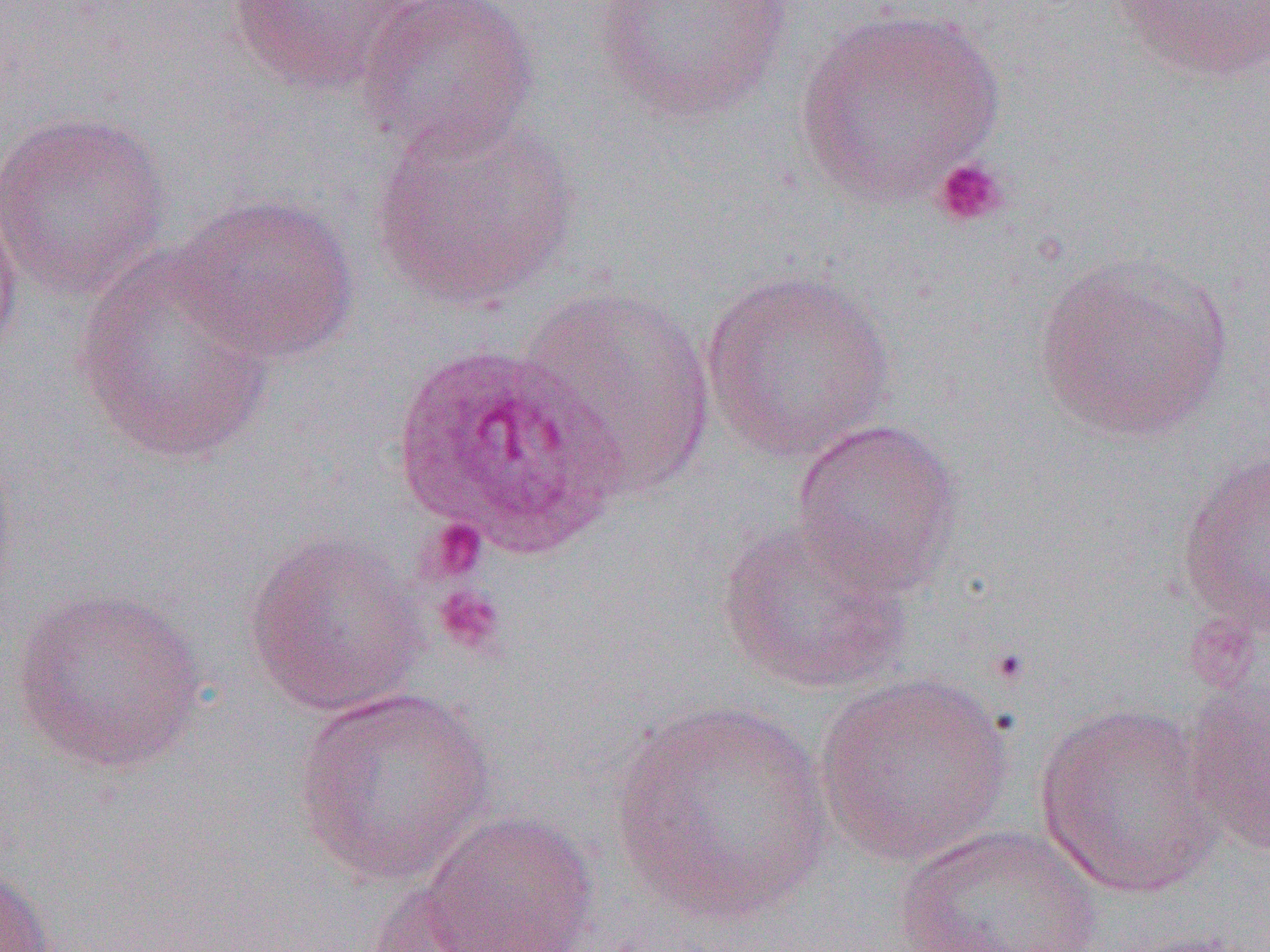

slide_level_diagnosis: Plasmodium ovale
magnification: 1000x
platelet_locations: 'approximate bounding boxes as named x1/y1/x2/y2 corners in pixels: (x1=930, y1=156, x2=1011, y2=229), (x1=422, y1=518, x2=488, y2=583), (x1=432, y1=584, x2=507, y2=657), (x1=985, y1=645, x2=1033, y2=689)'
field_of_view: one of a larger specimen
plasmodium_ovale_infected_red_blood_cell_locations: 'approximate bounding boxes as named x1/y1/x2/y2 corners in pixels: (x1=389, y1=342, x2=631, y2=560)'
preparation: thin blood smear
image_size: 1270×952 pixels
uninfected_red_blood_cell_locations: 'approximate bounding boxes as named x1/y1/x2/y2 corners in pixels: (x1=226, y1=0, x2=418, y2=96), (x1=356, y1=0, x2=540, y2=160), (x1=592, y1=0, x2=796, y2=123), (x1=1110, y1=0, x2=1269, y2=86), (x1=794, y1=5, x2=1006, y2=209), (x1=0, y1=110, x2=173, y2=299), (x1=368, y1=110, x2=580, y2=311), (x1=0, y1=185, x2=24, y2=367), (x1=170, y1=192, x2=361, y2=364), (x1=1032, y1=250, x2=1236, y2=444), (x1=73, y1=251, x2=277, y2=466), (x1=701, y1=267, x2=898, y2=461), (x1=517, y1=283, x2=717, y2=498), (x1=790, y1=417, x2=964, y2=598), (x1=0, y1=439, x2=20, y2=606), (x1=1175, y1=450, x2=1270, y2=637), (x1=717, y1=518, x2=912, y2=695), (x1=241, y1=531, x2=430, y2=718), (x1=11, y1=586, x2=207, y2=774), (x1=814, y1=671, x2=1013, y2=866), (x1=1183, y1=678, x2=1270, y2=859), (x1=292, y1=687, x2=495, y2=887), (x1=611, y1=699, x2=831, y2=927), (x1=1033, y1=702, x2=1224, y2=899), (x1=416, y1=809, x2=601, y2=952), (x1=893, y1=824, x2=1106, y2=951), (x1=0, y1=864, x2=56, y2=952), (x1=356, y1=878, x2=516, y2=951), (x1=1109, y1=929, x2=1267, y2=952)'
modality: optical microscopy